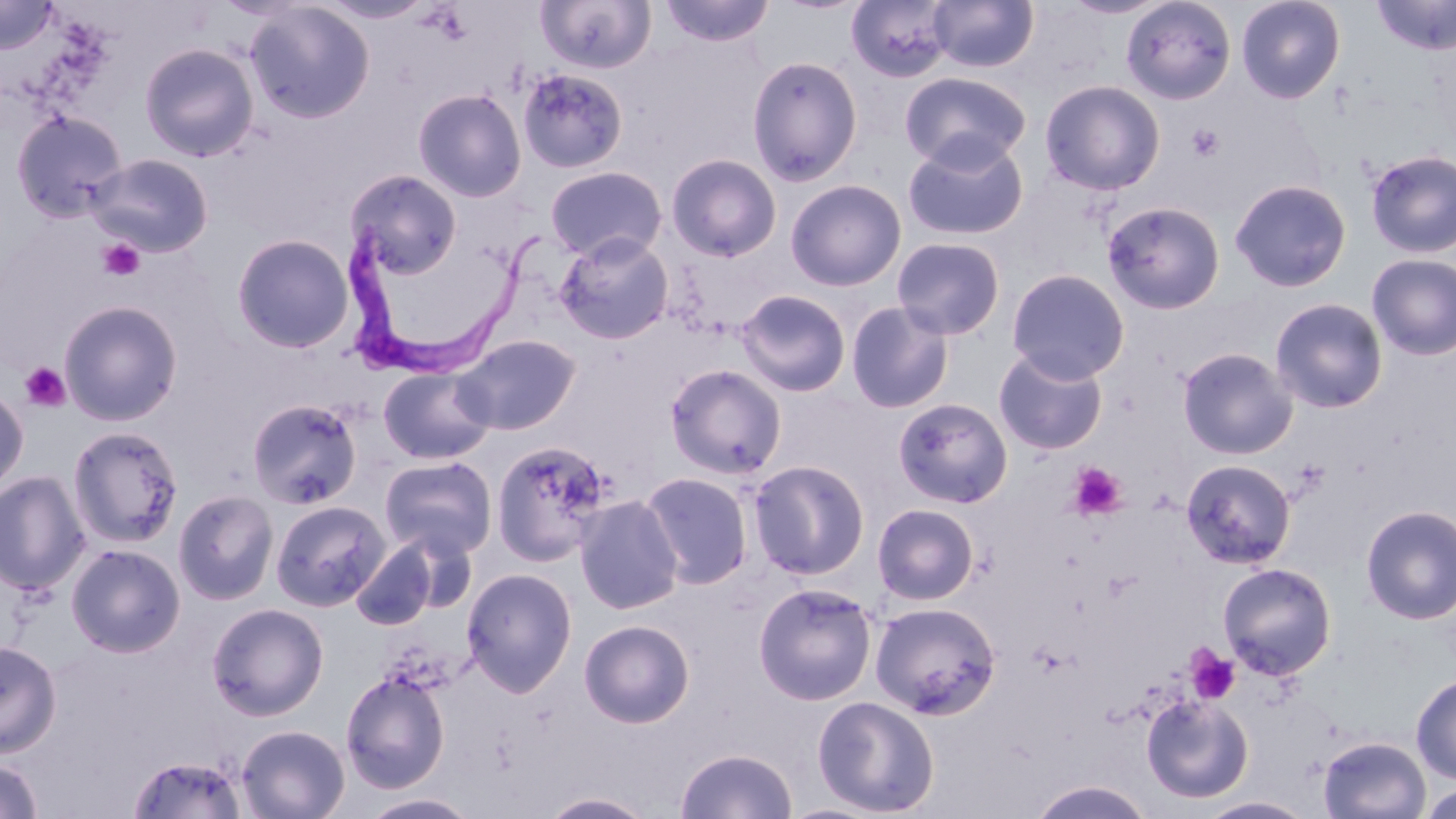

{
  "slide_level_diagnosis": "Trypanosoma brucei",
  "stain": "May-Grünwald-Giemsa",
  "magnification": "1000x",
  "preparation": "thin blood smear",
  "image_size": "1456×819 pixels",
  "modality": "light microscopy",
  "field_of_view": "one of a larger specimen",
  "trypanosoma_brucei_locations": "approximate bounding boxes as [x1, y1, x2, y2] in pixels: [340, 216, 555, 387]",
  "platelet_locations": "approximate bounding boxes as [x1, y1, x2, y2] in pixels: [1186, 124, 1225, 163], [97, 238, 145, 282], [20, 362, 71, 412], [1068, 461, 1126, 519], [1186, 647, 1241, 704]",
  "uninfected_red_blood_cell_locations": "approximate bounding boxes as [x1, y1, x2, y2] in pixels: [535, 0, 657, 74], [659, 0, 775, 47], [927, 0, 1039, 72], [1120, 0, 1238, 105], [1236, 0, 1345, 104], [1372, 0, 1456, 56], [0, 1, 60, 54], [846, 1, 954, 83], [243, 2, 376, 124], [139, 42, 259, 162], [746, 55, 864, 186], [517, 67, 628, 174], [899, 70, 1031, 171], [1040, 79, 1166, 195], [413, 87, 527, 202], [10, 109, 128, 223], [902, 134, 1030, 242], [1364, 148, 1456, 258], [89, 153, 214, 257], [666, 153, 782, 262], [544, 165, 668, 262], [345, 168, 463, 279], [1229, 178, 1351, 292], [784, 179, 907, 291], [1102, 200, 1226, 314], [554, 232, 675, 344], [231, 233, 355, 353], [891, 237, 1006, 340], [1367, 253, 1456, 360], [1006, 268, 1129, 384], [735, 289, 852, 397], [1269, 297, 1388, 413], [58, 299, 183, 426], [845, 300, 955, 413], [453, 334, 582, 435], [1177, 347, 1299, 460], [993, 348, 1108, 454], [664, 363, 787, 479], [377, 365, 496, 465], [0, 386, 29, 496], [893, 397, 1013, 509], [246, 398, 363, 509], [68, 425, 184, 548], [491, 440, 614, 566], [379, 455, 497, 559], [1180, 459, 1296, 569], [748, 460, 870, 580], [0, 471, 91, 596], [639, 472, 753, 588], [173, 488, 279, 605], [573, 494, 684, 614], [270, 499, 390, 611], [872, 503, 979, 605], [1359, 504, 1456, 625], [351, 540, 441, 630], [66, 543, 186, 657], [1217, 562, 1337, 680], [461, 567, 578, 697], [753, 582, 877, 705], [869, 601, 1002, 720], [206, 602, 329, 720], [578, 619, 695, 728], [0, 640, 62, 757], [340, 669, 451, 793], [1411, 672, 1456, 784], [1140, 694, 1254, 803], [812, 695, 940, 816], [236, 724, 350, 818], [1318, 735, 1431, 819], [674, 747, 797, 819], [126, 753, 249, 819], [0, 757, 44, 818], [1026, 779, 1157, 818], [1419, 783, 1456, 819], [538, 791, 659, 818], [358, 792, 482, 819], [1197, 796, 1316, 819]"
}